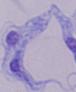
A trypanosome is shown. Photomicrograph. Captured at 1000x magnification.